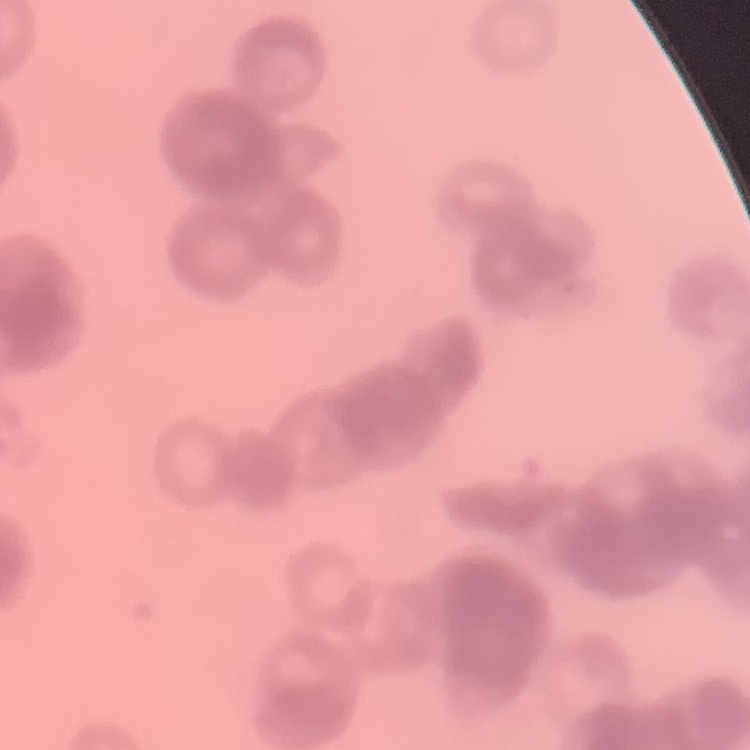
erythrocyte morphology = rouleaux formation
stain = Field's or Giemsa
image type = one tile cut from a larger photomicrograph
preparation = thin peripheral smear